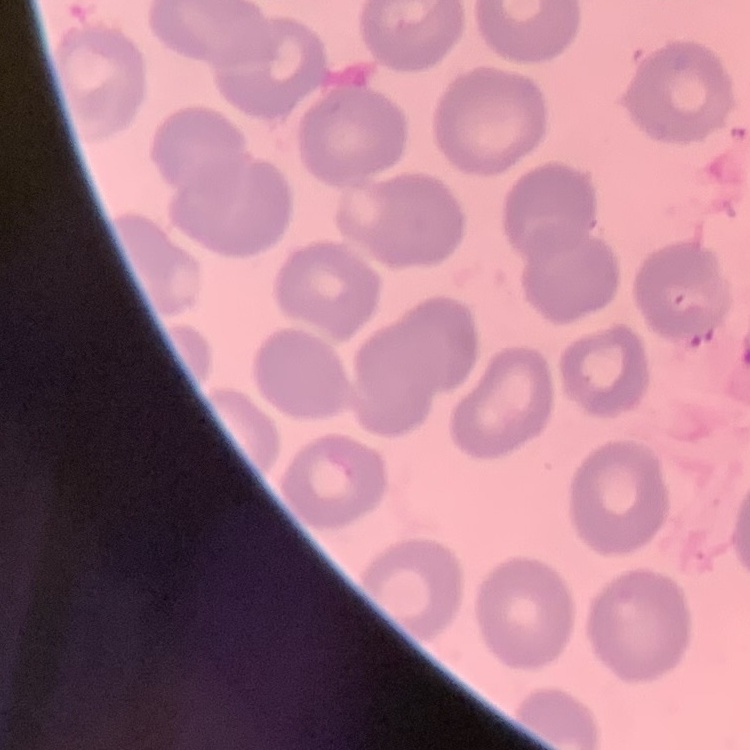 The red blood cells exhibit no rouleaux formation. Field's or Giemsa stain. Thin peripheral smear. One tile cut from a larger photomicrograph.